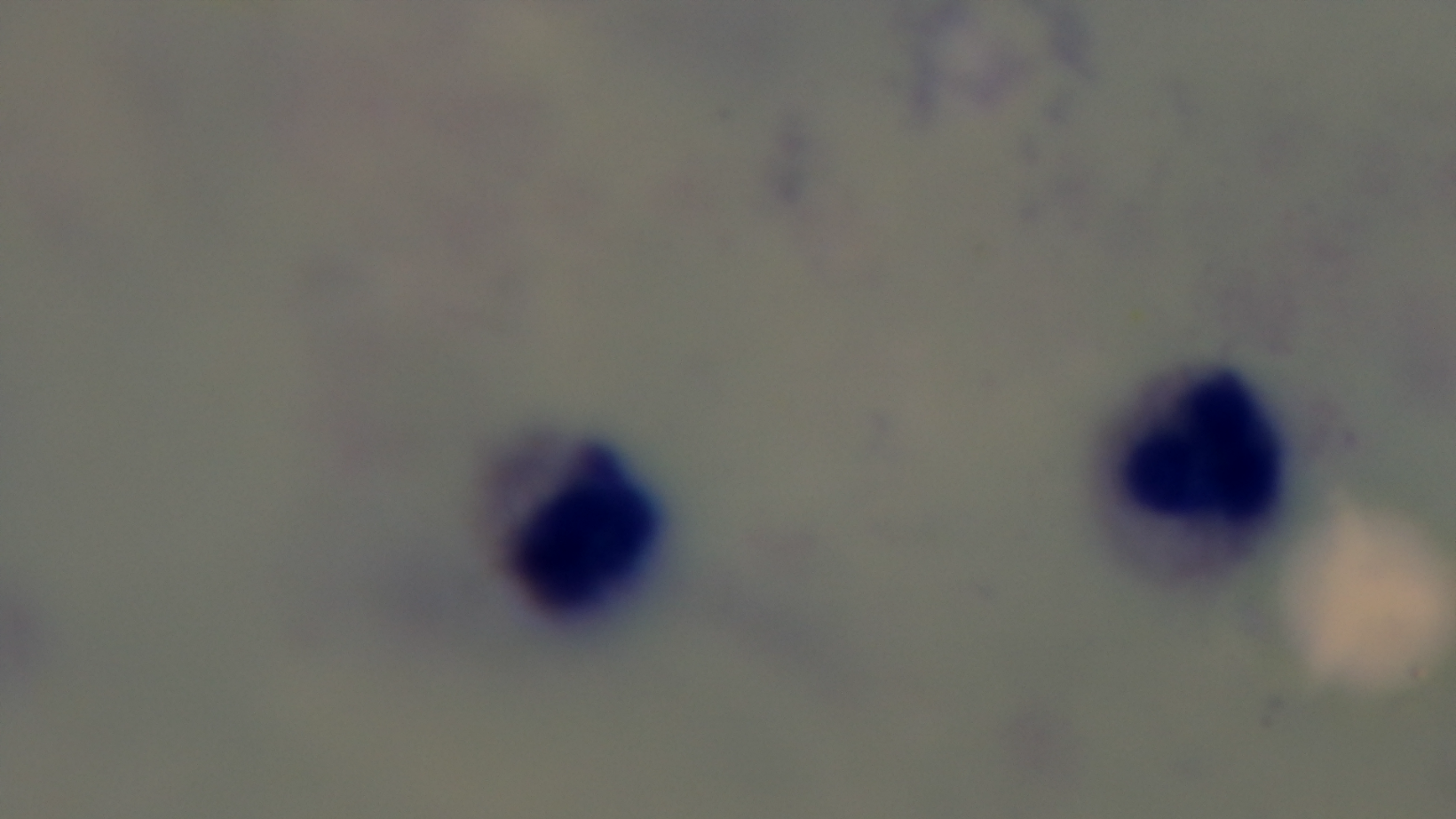 Giemsa-stained. Malaria status: negative. Captured with a mounted 4K digital camera. Preparation: thick blood film. Light microscopy. Single field of view. Oil-immersion objective, 100x.